State the blood parasite species.
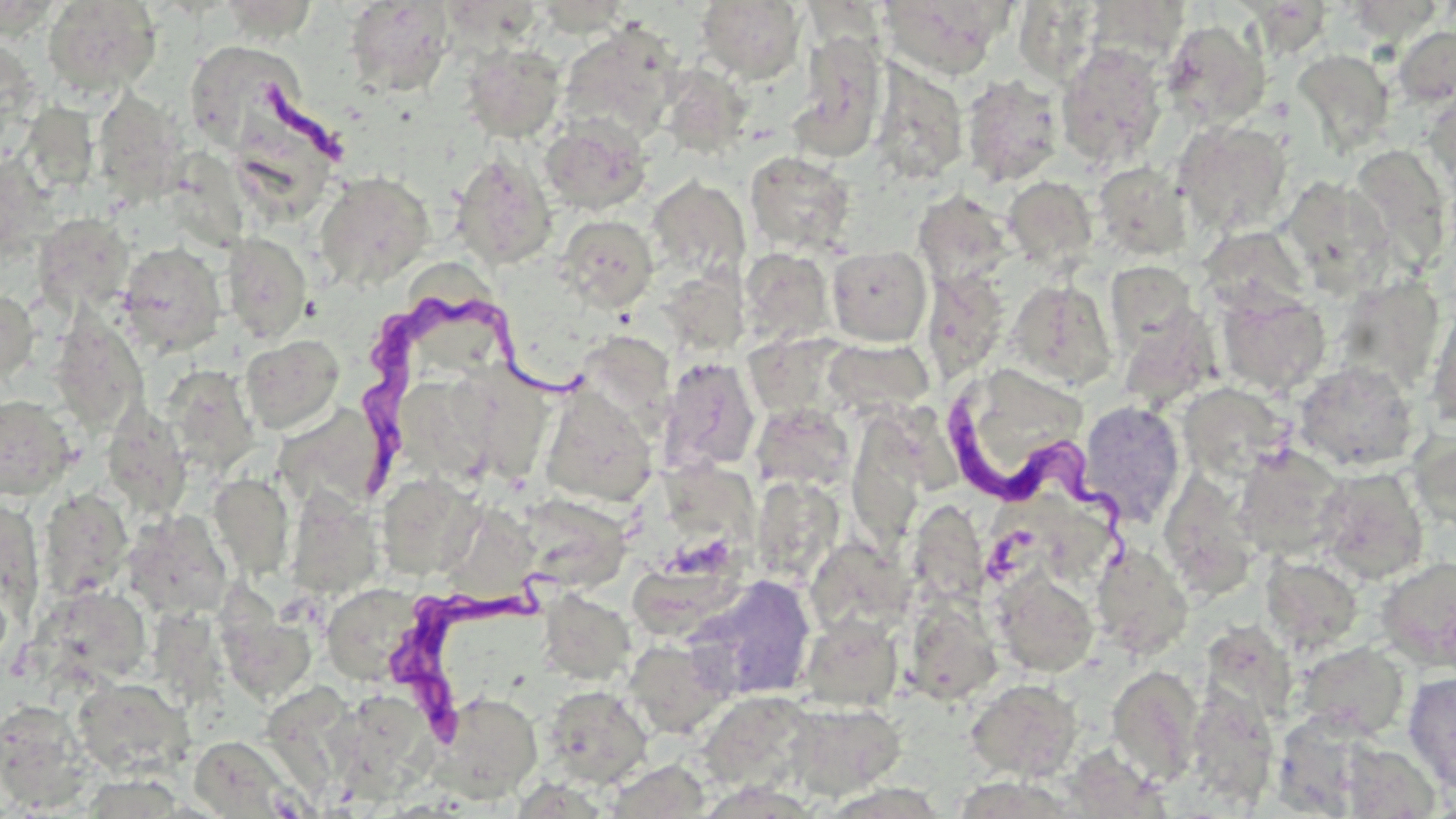
Trypanosoma brucei.

Approximate bounding boxes as [x1, y1, x2, y2] in pixels. Trypanosoma brucei locations: [357, 286, 593, 493], [941, 383, 1140, 585], [386, 558, 558, 741]. Uninfected red blood cell locations: [42, 0, 162, 97], [216, 0, 322, 42], [876, 0, 1015, 79], [1084, 0, 1190, 71], [344, 1, 454, 97], [696, 1, 807, 84], [1012, 2, 1106, 85], [1160, 19, 1271, 129], [559, 23, 681, 142], [1393, 25, 1456, 107], [790, 32, 887, 160], [0, 36, 40, 147], [186, 39, 303, 151], [460, 43, 567, 142], [1056, 43, 1167, 168], [1293, 50, 1395, 155], [869, 61, 969, 185], [656, 64, 751, 159], [961, 75, 1063, 188], [20, 86, 105, 200], [92, 89, 187, 207], [1422, 89, 1456, 193], [235, 96, 327, 206], [540, 116, 652, 216], [1173, 120, 1293, 237], [1347, 143, 1454, 274], [178, 151, 260, 250], [745, 151, 855, 255], [1, 153, 64, 270], [451, 154, 557, 270], [1093, 162, 1192, 262], [314, 171, 435, 290], [647, 176, 751, 284], [1003, 176, 1098, 271], [1279, 176, 1395, 292], [913, 189, 1014, 290], [32, 213, 134, 315], [556, 215, 658, 313], [1197, 224, 1310, 318], [222, 233, 311, 343], [116, 242, 227, 357], [826, 245, 932, 346], [739, 248, 834, 348], [1105, 261, 1199, 355], [418, 265, 501, 375], [922, 269, 1009, 382], [1332, 275, 1446, 393], [1006, 279, 1117, 392], [1215, 287, 1330, 397], [0, 289, 39, 384], [1428, 302, 1456, 430], [1117, 311, 1219, 410], [49, 315, 148, 435], [575, 331, 675, 435], [240, 335, 344, 434], [825, 337, 933, 415], [656, 357, 761, 477], [971, 362, 1101, 466], [1293, 362, 1419, 473], [162, 365, 259, 476], [457, 368, 556, 478], [409, 376, 488, 482], [1177, 383, 1291, 482], [540, 387, 657, 507], [0, 395, 77, 499], [1078, 401, 1186, 525], [752, 402, 855, 493], [272, 403, 391, 509], [101, 406, 192, 518], [846, 413, 930, 552], [1409, 430, 1456, 531], [1234, 444, 1348, 560], [1314, 468, 1429, 585], [668, 471, 761, 553], [208, 472, 293, 580], [1159, 473, 1259, 601], [376, 474, 481, 579], [280, 483, 385, 593], [38, 488, 133, 601], [767, 488, 842, 582], [514, 494, 632, 594], [0, 497, 45, 628], [453, 503, 543, 599], [120, 510, 232, 619], [804, 536, 915, 642], [1090, 539, 1193, 659], [1099, 541, 1197, 785], [1262, 555, 1363, 653], [1376, 557, 1455, 671], [639, 558, 760, 641], [991, 568, 1099, 678], [688, 574, 816, 701], [0, 578, 12, 673], [32, 584, 152, 688], [320, 584, 425, 686], [539, 590, 636, 684], [901, 594, 1003, 705], [218, 608, 319, 705], [799, 614, 903, 711], [1198, 621, 1298, 727], [624, 638, 735, 739], [1295, 641, 1409, 740], [1106, 664, 1204, 784], [1403, 671, 1456, 793], [71, 676, 194, 778], [966, 679, 1083, 781], [255, 683, 367, 810], [543, 684, 654, 787], [1183, 687, 1279, 808], [429, 690, 542, 802], [697, 691, 821, 796], [0, 699, 96, 811], [786, 700, 905, 799], [338, 702, 430, 798], [1271, 711, 1387, 814], [187, 735, 308, 818], [1063, 739, 1173, 817], [1338, 741, 1441, 817], [603, 761, 712, 817], [961, 765, 1066, 817]. One field of a larger specimen. May-Grünwald-Giemsa-stained preparation. Image is 1456×819 pixels. 1000x magnification. Optical microscopy. Thin blood smear.